Locate every Plasmodium vivax-infected red blood cell.
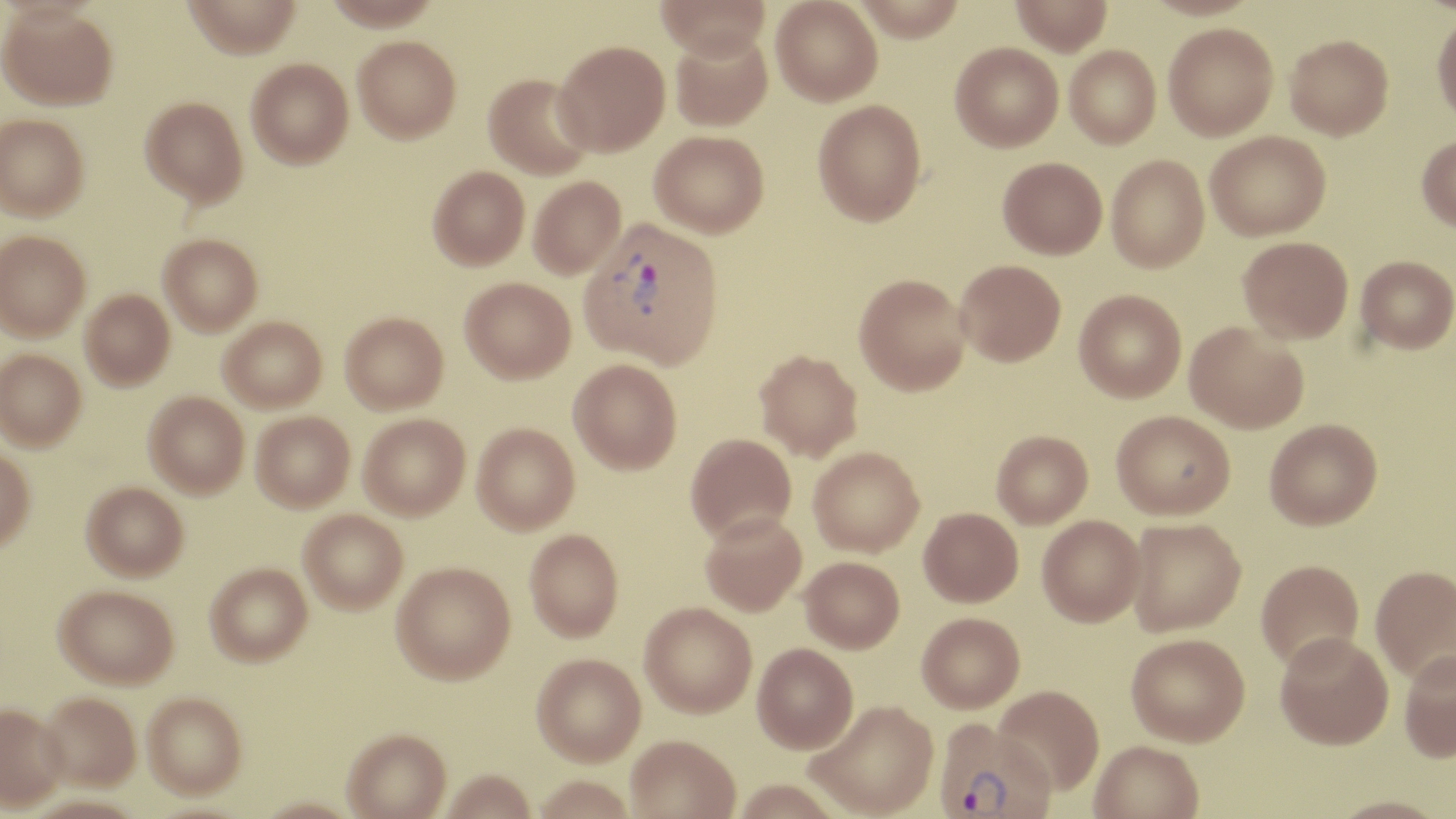

Approximate bounding boxes as (x1,y1)-(x2,y2) corner pairs in pixels.
Plasmodium vivax-infected red blood cells: (580,218)-(724,368), (933,722)-(1055,818).

slide_level_diagnosis: Plasmodium vivax
stain: May-Grünwald-Giemsa
modality: optical microscopy
field_of_view: one of a larger specimen
uninfected_red_blood_cell_locations: 'approximate bounding boxes as (x1,y1)-(x2,y2) corner pairs in pixels: (182,0)-(303,59), (656,0)-(770,61), (771,0)-(883,106), (852,0)-(966,42), (1010,0)-(1113,57), (1143,0)-(1261,20), (1,5)-(117,109), (1431,13)-(1456,126), (1163,23)-(1278,140), (671,30)-(772,131), (1285,34)-(1393,140), (353,36)-(461,142), (554,40)-(670,155), (950,42)-(1063,152), (1064,45)-(1161,149), (246,59)-(353,168), (484,72)-(595,179), (140,96)-(248,206), (813,100)-(927,226), (0,113)-(89,220), (649,130)-(769,238), (1205,130)-(1330,240), (1416,133)-(1456,232), (1106,154)-(1210,273), (997,156)-(1107,259), (428,165)-(530,269), (529,176)-(625,278), (0,230)-(90,340), (159,233)-(263,334), (1238,236)-(1353,343), (1355,255)-(1456,354), (955,259)-(1066,366), (854,273)-(971,395), (460,276)-(575,383), (80,289)-(175,390), (1074,289)-(1186,403), (340,311)-(448,413), (219,316)-(326,411), (1185,321)-(1309,434), (0,348)-(86,450), (754,350)-(863,461), (568,359)-(682,474), (144,390)-(249,497), (1111,410)-(1235,520), (251,411)-(355,511), (359,413)-(470,519), (1264,418)-(1382,530), (472,422)-(579,534), (991,430)-(1093,528), (685,433)-(796,543), (808,446)-(924,556), (0,447)-(35,552), (82,481)-(188,580), (919,507)-(1023,607), (299,509)-(408,613), (700,512)-(807,616), (1037,515)-(1146,627), (1126,518)-(1246,636), (525,528)-(623,641), (800,556)-(904,653), (1256,559)-(1364,674), (205,562)-(312,665), (391,562)-(515,684), (1370,565)-(1456,686), (55,584)-(178,688), (639,602)-(757,718), (917,612)-(1025,714), (1275,635)-(1394,754), (1126,636)-(1250,750), (752,645)-(859,755), (1399,651)-(1456,765), (532,653)-(646,765), (993,687)-(1104,799), (38,691)-(141,790), (143,691)-(247,798), (0,702)-(68,811), (806,702)-(938,819), (342,728)-(451,818), (626,736)-(740,819), (1090,744)-(1204,819), (440,769)-(537,819), (1325,798)-(1451,819)'
preparation: thin blood smear
magnification: 1000x
image_size: 1456×819 pixels